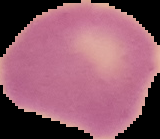

The area outside the segmented cell region is set to black. From a thin blood film. Malaria status: uninfected. Image is 160×139 pixels.